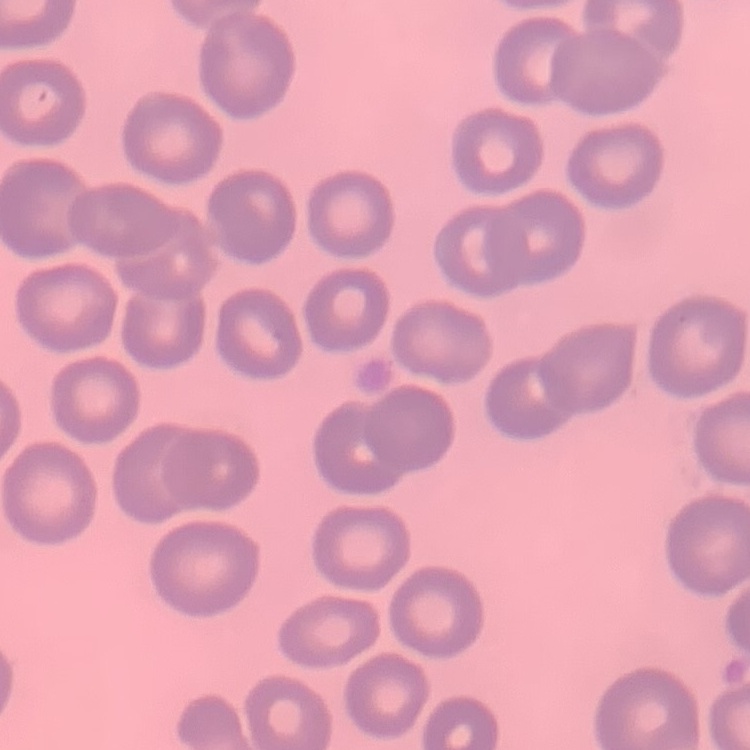 The erythrocytes exhibit no rouleaux formation. Thin blood film. One tile cut from a larger photomicrograph. Field's or Giemsa stain.